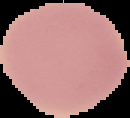

preparation: thin blood film
image_type: segmented cell region on a black background
image_size: 130×118 pixels
result: negative for malaria parasites